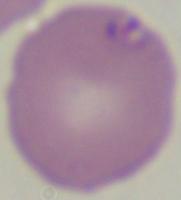

magnification = 1000x
modality = photomicrograph
identification = Babesia